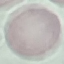

Summary:
  - Malaria status: uninfected
  - Preparation: thin smear
  - Stain: Giemsa
  - Capture: smartphone through the microscope eyepiece
  - Image type: cell patch, automatically extracted from a larger field of view and resized to 64 × 64 pixels